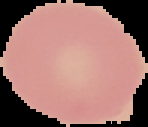 From a thin blood film. Segmented cell region on a black background. Image is 148×127 pixels. Malaria status: uninfected.